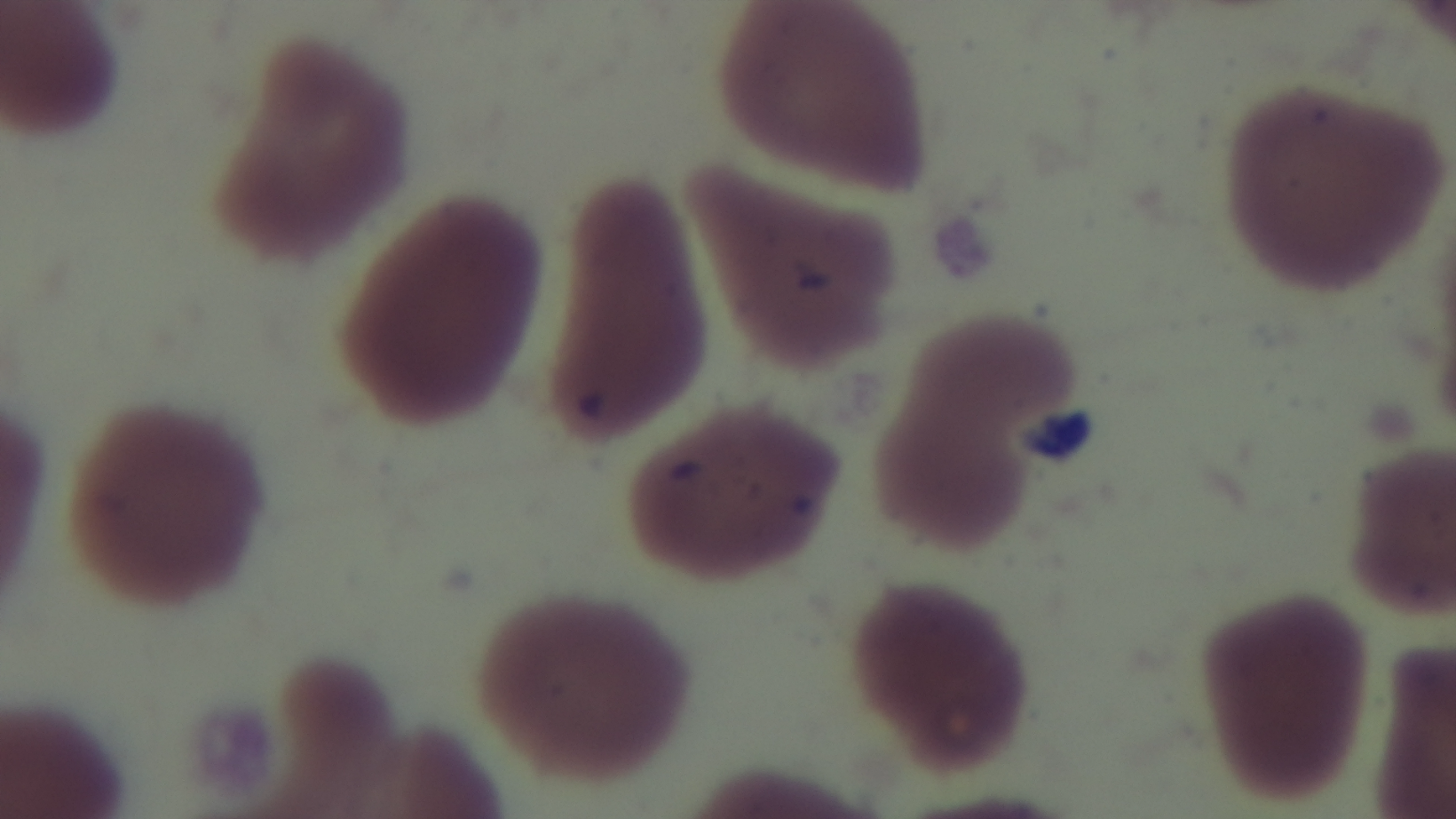 Photomicrograph. Oil-immersion objective, 100x. Single field of view. Captured with a mounted 4K digital camera. Preparation: thin blood film. Malaria status: uninfected. Giemsa stain.